Locate every Plasmodium parasite.
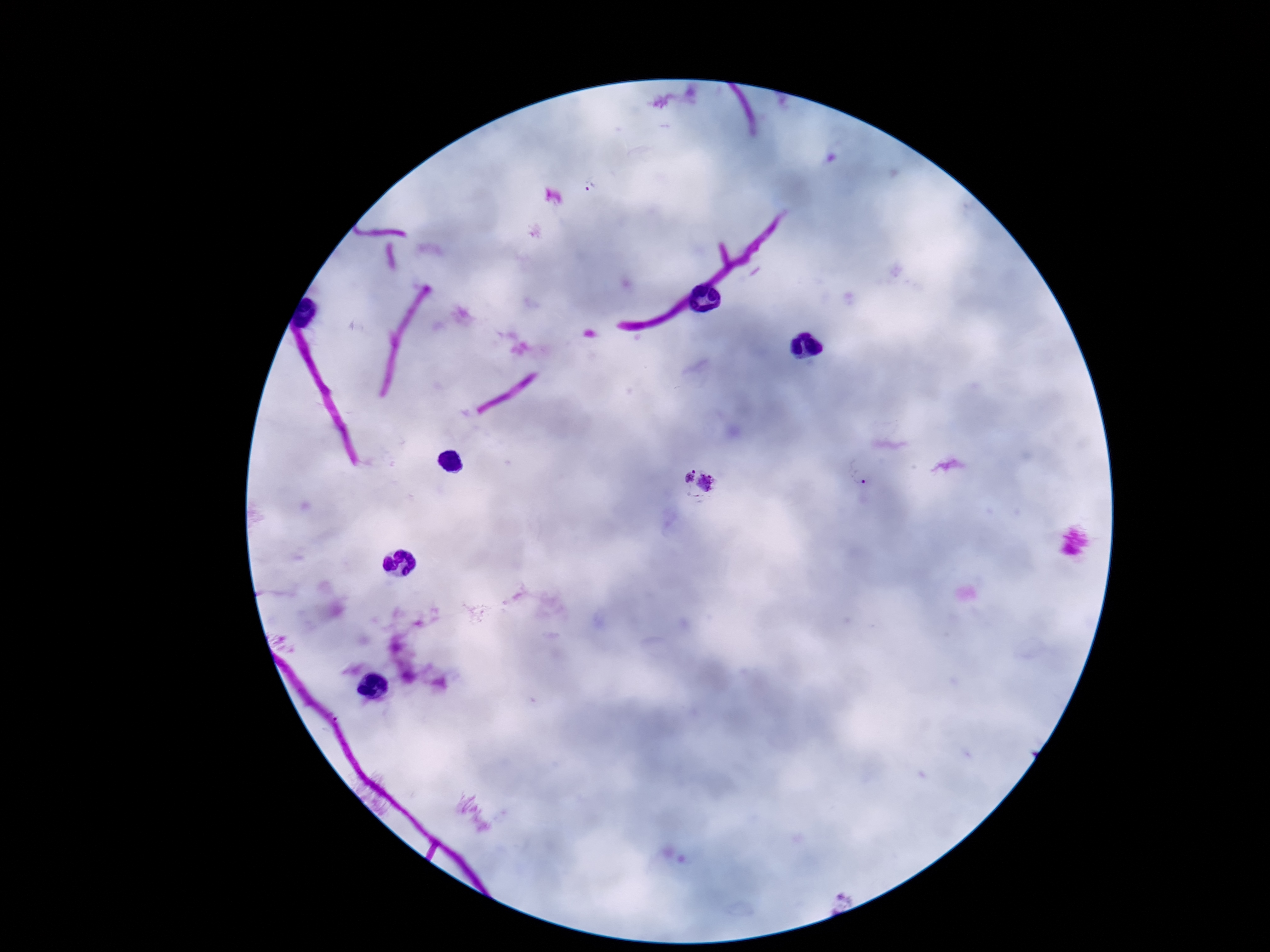
Approximate centers as (x, y) in pixels.
Plasmodium parasites: (592, 188), (860, 471), (698, 481).

magnification = 100x
preparation = thick peripheral-blood smear
capture = smartphone camera through the microscope eyepiece
field of view = one from this slide
patient malaria status = positive
image size = 1270×952 pixels
stain = Giemsa